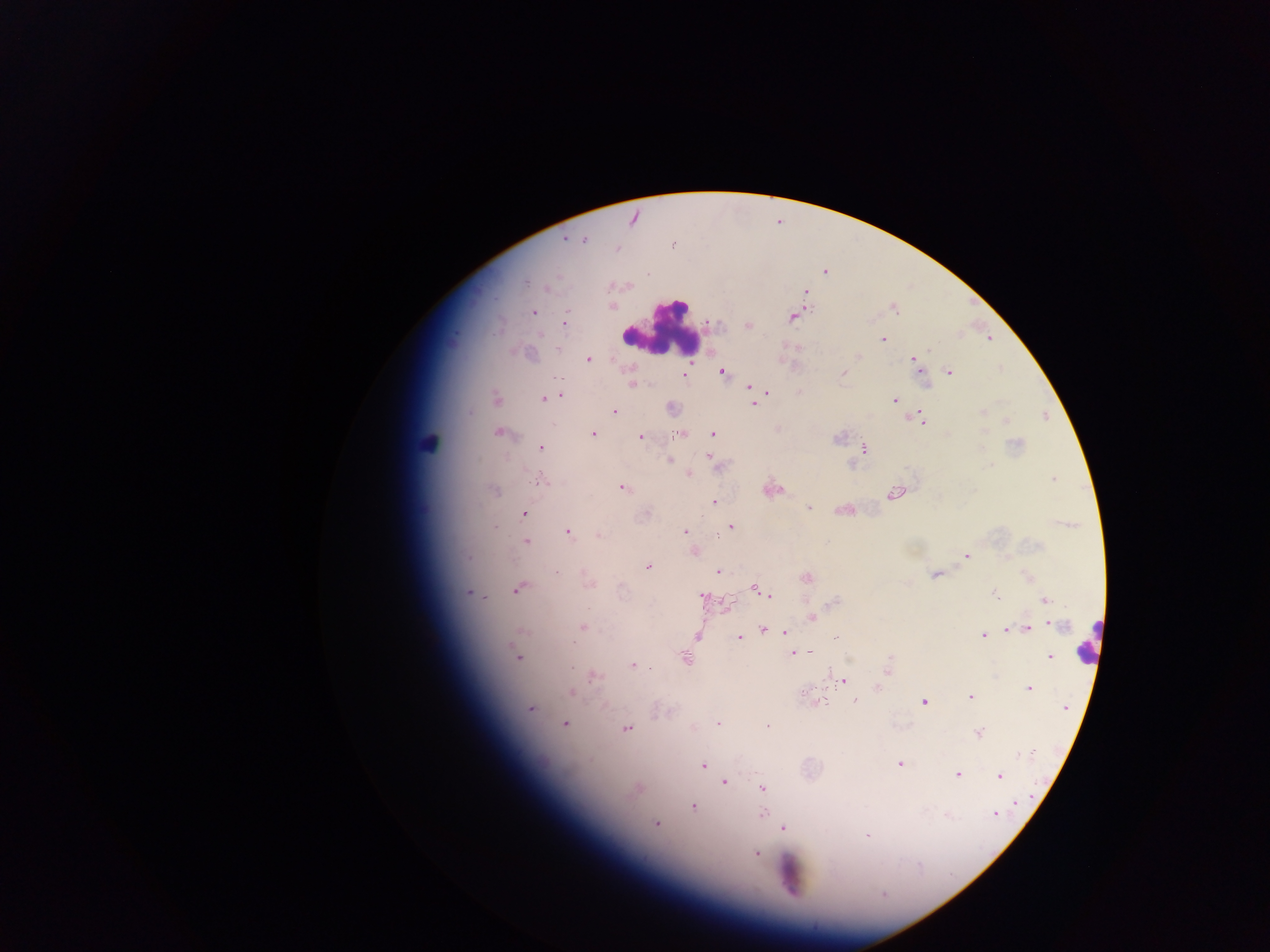
Approximate centers as (x, y) in pixels. Malaria parasite locations: (633, 217), (565, 238), (584, 240), (672, 245), (615, 249), (824, 272), (545, 288), (804, 290), (612, 306), (893, 307), (532, 312), (791, 317), (564, 323), (748, 325), (989, 338), (883, 339), (858, 356), (588, 358), (913, 360), (722, 371), (950, 372), (843, 373), (684, 375), (553, 378), (631, 385), (749, 386), (765, 390), (799, 391), (561, 395), (495, 398), (544, 399), (894, 400), (753, 403), (671, 407), (613, 411), (982, 411), (914, 417), (1004, 421), (923, 422), (499, 432), (592, 433), (712, 433), (679, 434), (640, 437), (837, 437), (540, 448), (863, 448), (709, 456), (669, 460), (851, 466), (686, 473), (540, 479), (1053, 479), (622, 487), (771, 488), (494, 491), (894, 493), (714, 503), (808, 507), (843, 510), (646, 513), (524, 514), (731, 526), (493, 527), (567, 531), (685, 532), (598, 535), (526, 542), (693, 551), (966, 556), (647, 566), (717, 571), (936, 574), (1027, 577), (806, 578), (588, 582), (518, 588), (754, 588), (468, 592), (763, 593), (994, 594), (768, 596), (702, 597), (1044, 599), (833, 602), (726, 604), (811, 617), (1051, 623), (583, 627), (1026, 628), (773, 629), (1004, 629), (764, 630), (522, 631), (785, 631), (982, 634), (697, 636), (740, 637), (837, 637), (811, 651), (791, 653), (517, 656), (1049, 657), (686, 659), (632, 663), (886, 669), (592, 675), (842, 679), (876, 687), (1028, 688), (571, 692), (970, 695), (855, 700), (924, 701), (817, 702), (529, 707), (1065, 707), (564, 724), (717, 724), (692, 725), (625, 727), (767, 727), (978, 732), (1033, 751), (703, 764), (899, 764), (956, 773), (999, 776), (724, 782), (637, 787), (762, 789), (1014, 803), (693, 807), (946, 813), (995, 813), (762, 814), (656, 823), (782, 827), (867, 835), (756, 852). Leukocyte locations: (662, 326), (431, 444), (1090, 642), (789, 876). Sample from Ghana. Single field of view. Mobile-phone photograph taken through the microscope. Thick blood smear. Image is 1270×952 pixels.